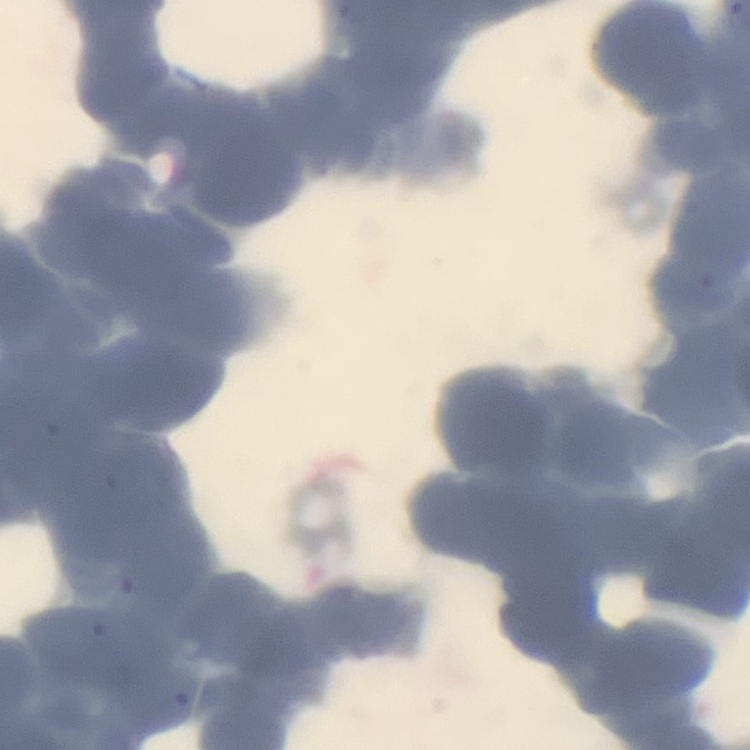

The erythrocytes exhibit rouleaux formation. One tile cut from a larger photomicrograph. Thin blood smear. Stained with either Field's or Giemsa.